Identify the parasite.
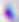
This is Toxoplasma gondii.

magnification = 400x
modality = photomicrograph